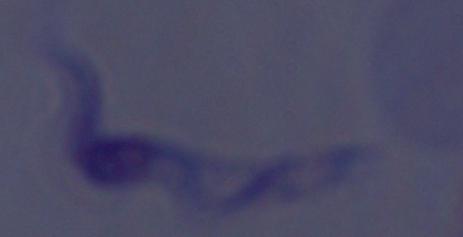

A trypanosome is seen. Photomicrograph. 1000x magnification.